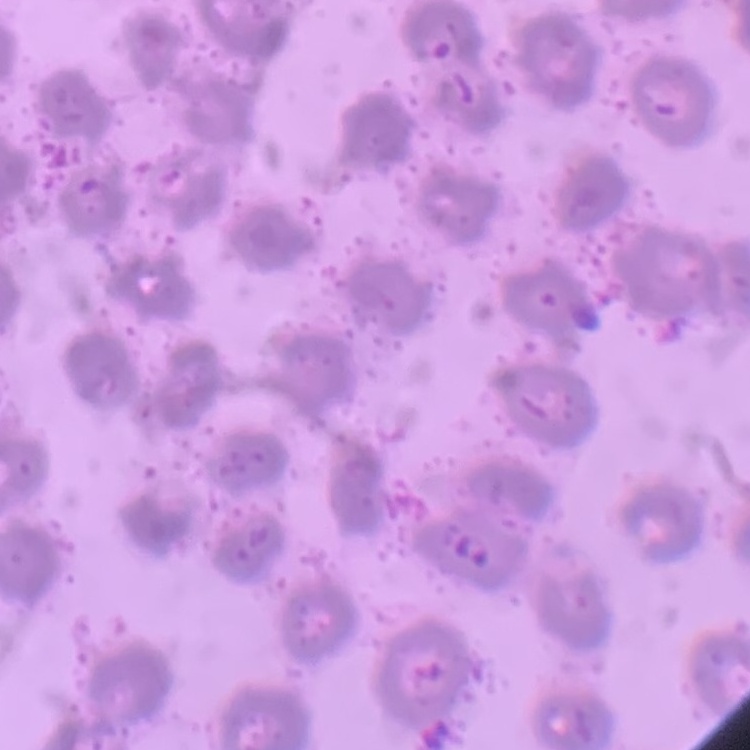

The erythrocytes exhibit no rouleaux formation. Thin peripheral smear. Stained with either Field's or Giemsa. Square crop of a larger photomicrograph.